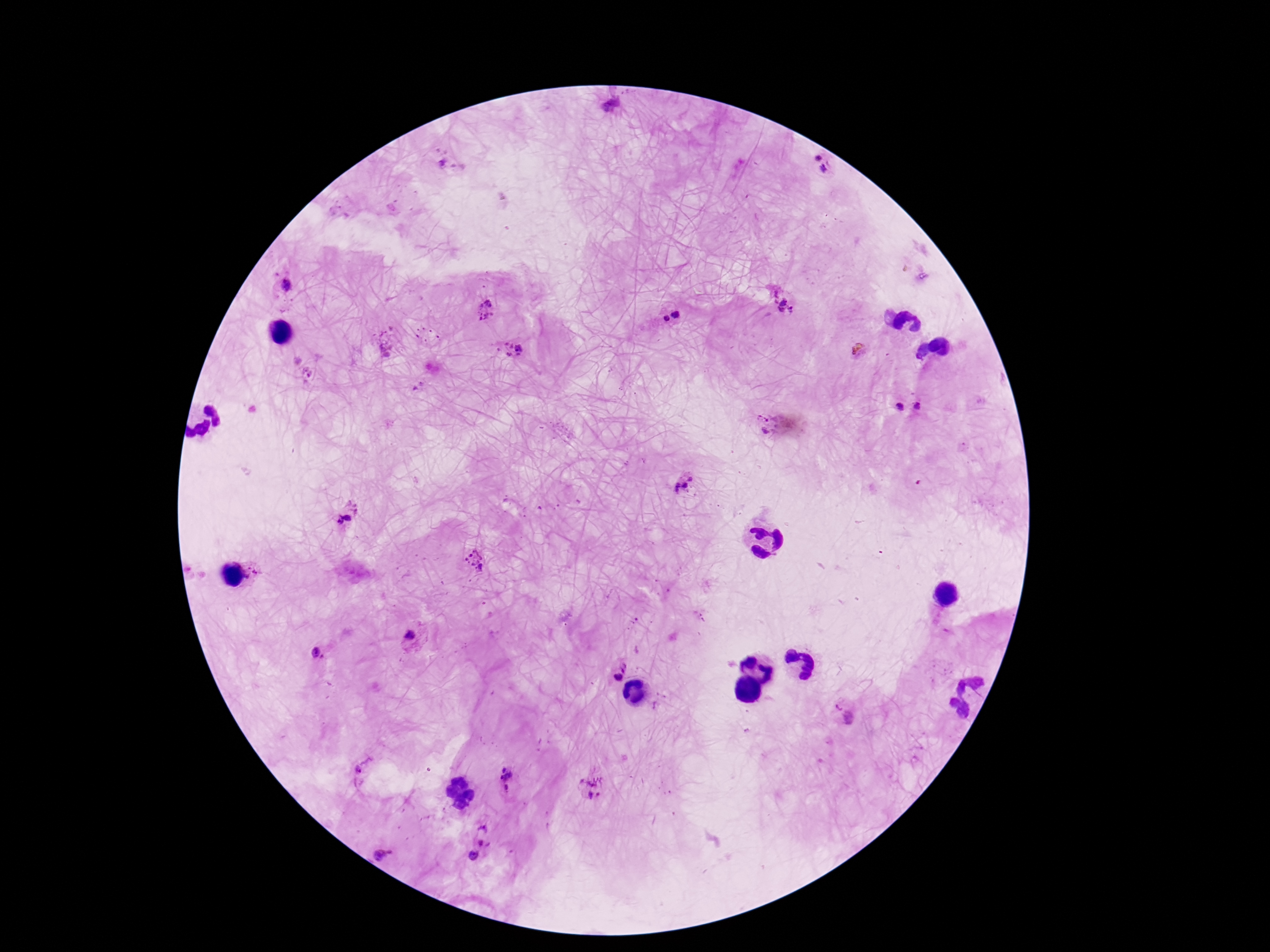

Approximate object centers, in pixels from the top-left corner.
Summary:
  - Plasmodium parasite locations: (x=611, y=106), (x=450, y=163), (x=819, y=169), (x=279, y=289), (x=783, y=302), (x=485, y=309), (x=670, y=314), (x=509, y=350), (x=917, y=406), (x=900, y=407), (x=759, y=423), (x=686, y=483), (x=344, y=514), (x=475, y=560), (x=259, y=573), (x=413, y=638), (x=318, y=653), (x=617, y=666), (x=839, y=703), (x=364, y=772), (x=507, y=779), (x=592, y=787), (x=488, y=836), (x=380, y=855), (x=472, y=858)
  - Magnification: 100x
  - Field of view: one from this slide
  - Stain: Giemsa
  - Image size: 1270×952 pixels
  - Patient malaria status: positive
  - Capture: smartphone camera through the microscope eyepiece
  - Preparation: thick peripheral-blood smear